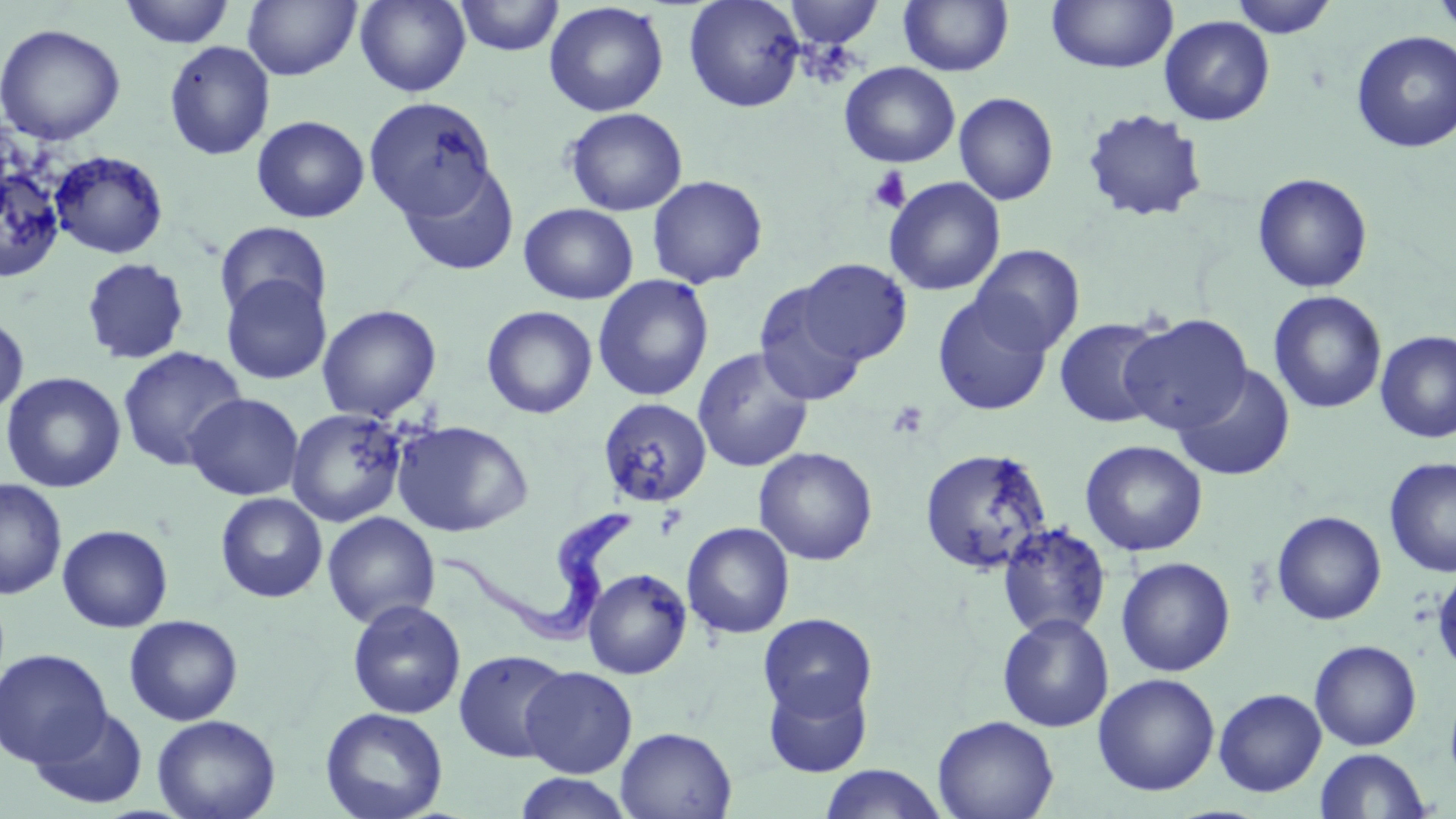
Summary:
  - Coordinate format: approximate bounding boxes as (x1, y1, x2, y2) in pixels
  - Uninfected red blood cell locations: (117, 0, 238, 48), (355, 0, 470, 96), (454, 0, 565, 57), (683, 0, 805, 112), (899, 0, 1014, 77), (1047, 0, 1177, 73), (1228, 0, 1339, 39), (1430, 0, 1456, 37), (242, 1, 362, 81), (544, 1, 669, 117), (784, 1, 884, 48), (1159, 15, 1275, 126), (0, 23, 126, 145), (1351, 30, 1456, 153), (164, 41, 275, 161), (839, 61, 960, 168), (954, 92, 1059, 206), (364, 95, 498, 220), (1081, 107, 1208, 223), (564, 108, 687, 216), (251, 115, 370, 223), (0, 139, 69, 287), (48, 150, 169, 259), (395, 161, 520, 277), (1252, 173, 1373, 293), (646, 175, 768, 289), (883, 176, 1005, 296), (518, 203, 638, 304), (214, 221, 332, 324), (971, 244, 1085, 356), (80, 257, 191, 365), (797, 258, 911, 365), (221, 273, 332, 386), (592, 274, 714, 403), (753, 281, 868, 407), (1268, 290, 1387, 415), (933, 293, 1053, 416), (317, 304, 441, 421), (481, 305, 597, 419), (1119, 314, 1253, 433), (0, 316, 29, 417), (1054, 318, 1168, 428), (1375, 330, 1456, 443), (117, 346, 248, 471), (692, 347, 814, 473), (1173, 364, 1295, 481), (1, 371, 126, 493), (184, 392, 304, 501), (597, 397, 712, 508), (286, 407, 411, 527), (393, 420, 533, 537), (1080, 440, 1208, 556), (753, 446, 877, 565), (919, 447, 1053, 575), (1384, 456, 1456, 579), (0, 479, 67, 600), (215, 492, 328, 603), (1271, 510, 1387, 626), (322, 511, 440, 629), (682, 522, 795, 639), (997, 522, 1111, 641), (57, 524, 173, 632), (1116, 556, 1236, 677), (1432, 566, 1456, 677), (583, 567, 692, 679), (347, 600, 466, 720), (758, 613, 877, 721), (997, 613, 1114, 732), (123, 614, 244, 726), (144, 617, 259, 819), (1309, 640, 1422, 751), (0, 648, 112, 767), (453, 649, 573, 763), (520, 666, 637, 778), (1093, 673, 1220, 796), (763, 675, 872, 778), (1214, 688, 1327, 797), (29, 706, 148, 810), (320, 707, 449, 819), (152, 714, 280, 819), (932, 715, 1059, 819), (616, 726, 737, 819), (1314, 747, 1431, 819), (819, 764, 948, 819), (513, 772, 634, 818)
  - Trypanosoma brucei locations: (437, 501, 635, 647)
  - Platelet locations: (867, 167, 912, 214), (886, 400, 930, 440), (655, 504, 689, 540)
  - Slide-level diagnosis: Trypanosoma brucei
  - Modality: light microscopy
  - Magnification: 1000x
  - Field of view: one of a larger specimen
  - Image size: 1456×819 pixels
  - Stain: May-Grünwald-Giemsa
  - Preparation: thin blood film